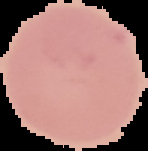 From a thin blood smear. Malaria status: uninfected. Cell region segmented out of the field of view; the surrounding area is masked to black. Image is 148×151 pixels.